Outline each blood parasite and name the species.
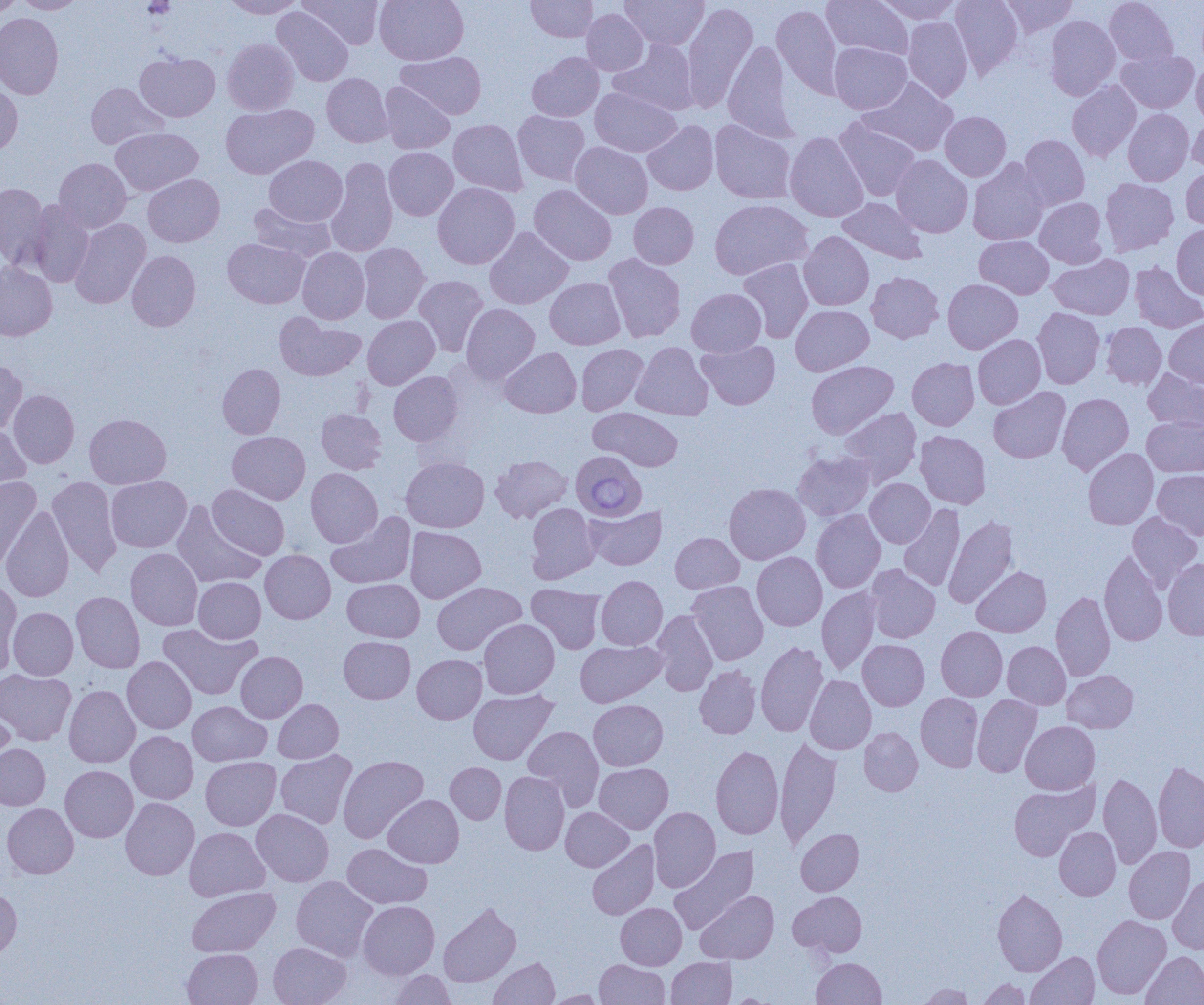
Approximate bounding boxes as [x1, y1, x2, y2] in pixels.
Babesia divergens-infected red blood cells: [567, 453, 649, 520].
No Plasmodium falciparum, Plasmodium ovale, Plasmodium malariae, Plasmodium vivax, or Trypanosoma brucei observed.

Summary:
  - Uninfected red blood cell locations: [0, 0, 21, 19], [220, 0, 305, 18], [300, 0, 383, 48], [374, 0, 468, 65], [526, 0, 598, 41], [621, 0, 709, 50], [822, 0, 913, 59], [874, 0, 961, 23], [950, 0, 1024, 78], [1000, 0, 1078, 37], [1104, 0, 1178, 66], [14, 1, 86, 14], [682, 2, 758, 113], [771, 4, 843, 98], [271, 6, 353, 86], [581, 9, 649, 76], [0, 13, 63, 99], [1044, 15, 1120, 100], [903, 16, 972, 101], [222, 39, 299, 115], [610, 39, 699, 115], [723, 39, 797, 141], [829, 42, 912, 114], [1116, 49, 1199, 113], [397, 51, 486, 119], [135, 52, 220, 122], [527, 52, 604, 122], [1191, 60, 1204, 126], [322, 73, 393, 147], [859, 77, 958, 156], [1067, 80, 1141, 162], [0, 82, 23, 156], [379, 82, 455, 154], [86, 83, 167, 150], [590, 87, 681, 157], [221, 104, 318, 179], [1123, 109, 1194, 186], [513, 111, 590, 186], [940, 111, 1011, 181], [1187, 113, 1204, 172], [834, 117, 920, 201], [448, 119, 528, 196], [710, 119, 796, 204], [642, 120, 719, 195], [111, 127, 203, 196], [784, 131, 869, 222], [1019, 134, 1089, 210], [570, 142, 653, 218], [384, 147, 458, 220], [891, 154, 973, 237], [264, 155, 347, 226], [325, 157, 398, 257], [54, 158, 131, 233], [968, 158, 1049, 245], [1181, 166, 1204, 231], [143, 174, 224, 247], [1100, 178, 1179, 255], [0, 182, 49, 267], [433, 182, 520, 269], [529, 184, 616, 265], [838, 197, 927, 264], [1035, 197, 1107, 268], [28, 199, 94, 288], [710, 199, 813, 279], [628, 202, 698, 269], [248, 203, 336, 262], [70, 219, 150, 308], [1172, 224, 1204, 300], [484, 227, 573, 309], [799, 231, 874, 310], [974, 235, 1054, 299], [223, 238, 310, 308], [358, 243, 430, 323], [297, 247, 369, 324], [127, 250, 201, 331], [603, 253, 686, 343], [1048, 254, 1134, 319], [737, 258, 814, 343], [0, 262, 57, 341], [1129, 262, 1204, 333], [866, 271, 944, 343], [414, 275, 488, 356], [545, 277, 625, 349], [943, 279, 1023, 353], [687, 288, 766, 357], [461, 304, 539, 385], [790, 305, 873, 375], [1033, 307, 1105, 389], [274, 313, 366, 381], [363, 315, 439, 389], [1164, 317, 1204, 388], [1101, 321, 1167, 390], [973, 334, 1046, 409], [697, 339, 780, 409], [631, 342, 713, 420], [576, 344, 648, 415], [500, 347, 581, 417], [907, 357, 979, 430], [0, 359, 27, 435], [806, 360, 899, 439], [217, 363, 285, 439], [1143, 368, 1204, 432], [388, 371, 463, 445], [988, 387, 1070, 463], [8, 389, 79, 468], [1057, 393, 1134, 475], [588, 407, 683, 471], [838, 407, 922, 486], [317, 408, 386, 474], [85, 414, 171, 489], [1143, 417, 1204, 476], [0, 421, 31, 500], [227, 431, 310, 504], [915, 431, 991, 509], [1083, 448, 1158, 529], [793, 451, 875, 521], [490, 455, 573, 523], [401, 457, 489, 532], [305, 468, 382, 547], [1153, 469, 1204, 540], [0, 476, 42, 569], [47, 476, 123, 577], [106, 476, 192, 552], [865, 478, 935, 547], [724, 482, 810, 564], [207, 484, 289, 560], [172, 502, 266, 589], [526, 503, 600, 583], [898, 504, 965, 591], [584, 505, 667, 570], [1, 507, 75, 602], [812, 509, 885, 592], [326, 511, 416, 589], [1127, 511, 1202, 592], [944, 515, 1018, 609], [405, 526, 486, 603], [670, 532, 743, 593], [126, 547, 203, 630], [260, 550, 335, 624], [1099, 550, 1168, 646], [752, 552, 827, 630], [1163, 558, 1204, 639], [866, 565, 940, 643], [971, 566, 1051, 637], [596, 575, 668, 650], [193, 577, 266, 643], [0, 578, 22, 673], [343, 578, 424, 642], [687, 580, 768, 665], [432, 582, 526, 655], [527, 585, 606, 654], [817, 587, 881, 675], [72, 591, 145, 673], [1051, 592, 1115, 681], [8, 607, 78, 680], [651, 610, 718, 696], [478, 619, 559, 698], [158, 624, 261, 700], [936, 626, 1007, 701], [339, 636, 415, 704], [858, 639, 929, 710], [575, 640, 666, 707], [756, 641, 829, 736], [1002, 641, 1070, 709], [236, 651, 307, 722], [412, 654, 486, 724], [122, 656, 196, 734], [694, 665, 761, 739], [0, 669, 76, 745], [1063, 670, 1138, 732], [805, 675, 876, 754], [64, 685, 140, 768], [468, 689, 557, 765], [915, 693, 983, 772], [972, 694, 1042, 777], [273, 699, 343, 763], [0, 700, 15, 773], [588, 700, 668, 771], [187, 701, 271, 766], [1020, 721, 1100, 794], [523, 726, 604, 809], [859, 727, 923, 795], [126, 731, 198, 804], [775, 736, 842, 848], [0, 743, 50, 810], [710, 745, 783, 839], [276, 750, 357, 828], [338, 755, 428, 843], [201, 756, 281, 830], [1153, 761, 1204, 853], [446, 762, 506, 824], [594, 763, 673, 834], [60, 765, 138, 842], [499, 771, 570, 855], [1098, 772, 1161, 869], [1008, 780, 1098, 861], [383, 794, 464, 868], [120, 797, 199, 880], [2, 803, 78, 878], [561, 807, 634, 871], [649, 807, 720, 892], [251, 809, 334, 886], [1054, 826, 1120, 900], [185, 827, 270, 900], [796, 829, 863, 895], [587, 840, 660, 919], [342, 843, 431, 908], [669, 846, 758, 935], [1124, 846, 1195, 924], [1168, 874, 1204, 953], [291, 876, 378, 961], [0, 885, 22, 960], [187, 887, 280, 957], [993, 888, 1067, 976], [696, 891, 778, 964], [788, 891, 867, 956], [357, 900, 439, 979], [438, 902, 521, 987], [616, 902, 686, 970], [1092, 915, 1171, 1000], [268, 942, 351, 1005], [182, 948, 262, 1005], [1026, 951, 1099, 1005], [1141, 951, 1204, 1004], [489, 957, 559, 1004], [666, 957, 736, 1005], [812, 958, 886, 1005], [594, 959, 669, 1004], [387, 970, 455, 1004], [977, 978, 1030, 1004], [918, 984, 974, 1004], [546, 989, 607, 1004], [725, 993, 780, 1004]
  - Slide-level diagnosis: Babesia divergens
  - Image size: 1204×1005 pixels
  - Field of view: one of a larger specimen
  - Preparation: thin blood smear
  - Magnification: 1000x
  - Modality: light microscopy